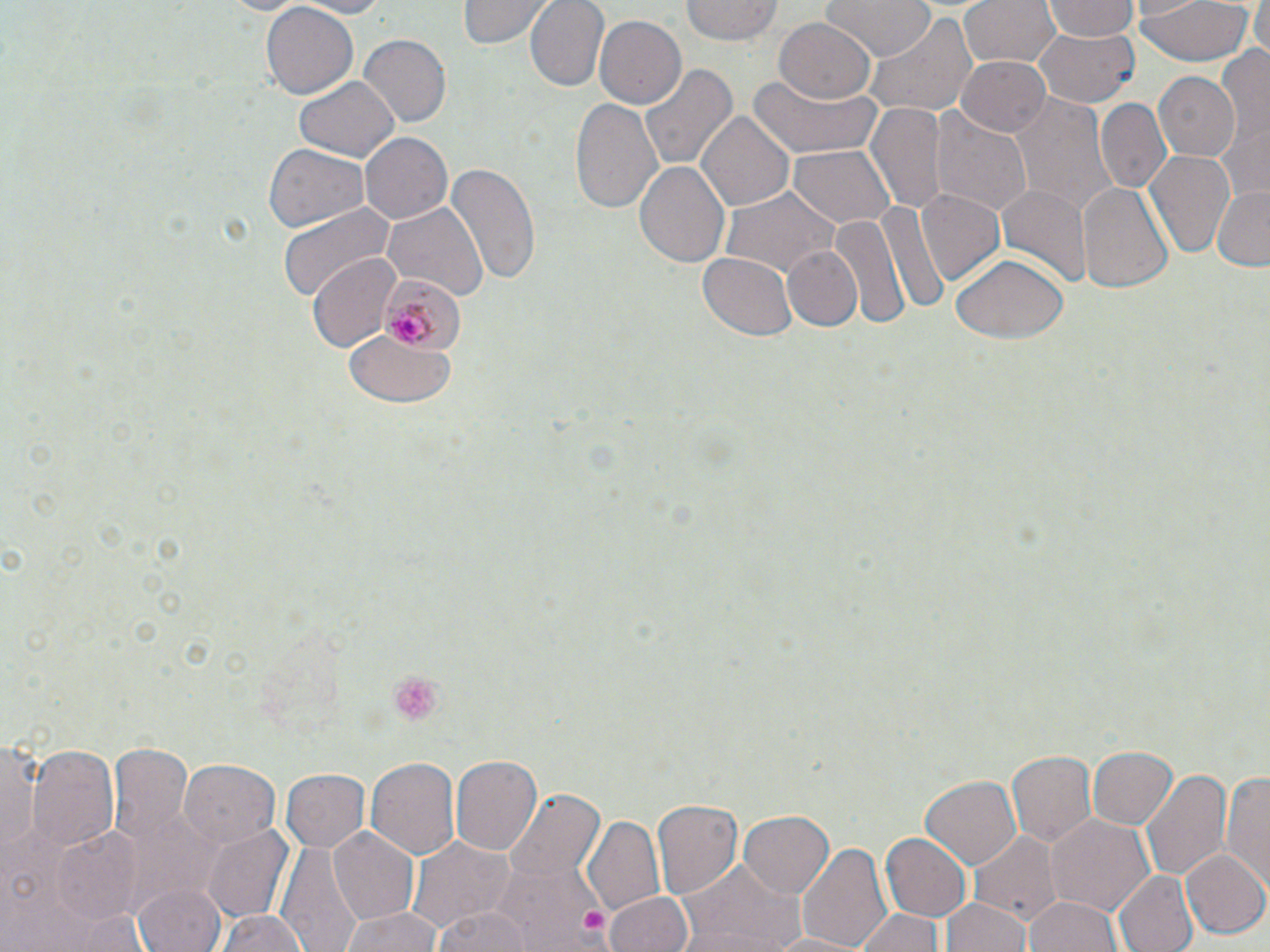

{
  "slide_level_diagnosis": "Plasmodium malariae",
  "modality": "light microscopy",
  "platelet_locations": "approximate bounding boxes as [x1, y1, x2, y2] in pixels: [386, 671, 446, 727], [582, 905, 608, 931]",
  "plasmodium_malariae_infected_red_blood_cell_locations": "approximate bounding boxes as [x1, y1, x2, y2] in pixels: [380, 272, 463, 355]",
  "field_of_view": "one of a larger specimen",
  "image_size": "1270×952 pixels",
  "stain": "May-Grünwald-Giemsa",
  "preparation": "thin blood film",
  "magnification": "1000x",
  "uninfected_red_blood_cell_locations": "approximate bounding boxes as [x1, y1, x2, y2] in pixels: [285, 0, 395, 16], [457, 0, 551, 48], [524, 0, 609, 91], [679, 0, 781, 45], [824, 0, 936, 61], [958, 0, 1061, 72], [1134, 0, 1256, 67], [1249, 0, 1270, 60], [262, 1, 358, 97], [1042, 2, 1141, 43], [862, 13, 979, 120], [593, 15, 686, 109], [773, 19, 876, 105], [1033, 23, 1140, 106], [358, 33, 450, 126], [1216, 44, 1270, 142], [956, 55, 1050, 137], [639, 62, 735, 174], [751, 70, 881, 158], [1153, 72, 1240, 164], [293, 73, 400, 162], [1006, 92, 1116, 210], [571, 97, 663, 214], [1094, 99, 1173, 194], [867, 102, 947, 212], [931, 110, 1032, 216], [698, 111, 794, 211], [1218, 116, 1270, 200], [359, 132, 452, 224], [261, 143, 370, 233], [786, 144, 895, 230], [1143, 150, 1235, 261], [635, 158, 732, 269], [445, 161, 540, 285], [1076, 180, 1171, 294], [999, 181, 1092, 286], [1211, 185, 1270, 270], [721, 188, 839, 278], [917, 190, 1006, 285], [876, 199, 951, 320], [383, 200, 487, 302], [279, 204, 394, 301], [829, 207, 909, 331], [782, 245, 861, 332], [696, 252, 798, 341], [307, 253, 403, 351], [948, 253, 1067, 342], [348, 333, 455, 405], [1, 731, 40, 862], [109, 740, 193, 850], [28, 743, 119, 854], [1086, 746, 1179, 831], [1007, 750, 1099, 848], [451, 756, 543, 858], [367, 757, 461, 859], [181, 761, 279, 849], [280, 768, 369, 853], [1143, 768, 1228, 884], [1224, 768, 1270, 890], [920, 775, 1023, 869], [504, 790, 603, 887], [651, 800, 743, 899], [738, 810, 833, 899], [582, 816, 667, 918], [1045, 816, 1155, 922], [202, 826, 294, 921], [327, 826, 418, 925], [50, 828, 145, 925], [971, 830, 1060, 924], [882, 832, 971, 919], [407, 836, 515, 933], [799, 841, 894, 952], [276, 844, 366, 952], [1181, 849, 1270, 940], [483, 859, 605, 950], [680, 859, 800, 951], [1112, 870, 1199, 952], [135, 883, 226, 952], [603, 892, 694, 952], [1026, 894, 1121, 952], [945, 896, 1030, 952], [339, 905, 444, 952], [430, 907, 539, 952], [853, 907, 947, 952], [215, 910, 312, 952], [755, 930, 876, 951]"
}